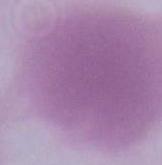
Summary:
  - Modality: micrograph
  - Identification: erythrocyte
  - Magnification: 1000x